Assess this cell for malaria.
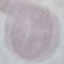

Uninfected.

Summary:
  - Image type: automatically extracted cell patch, resized to 64 × 64 pixels
  - Stain: Giemsa
  - Capture: smartphone through the microscope eyepiece
  - Preparation: thin blood film